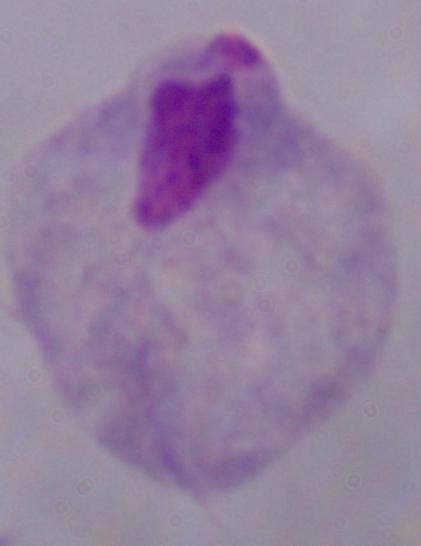

Summary:
  - Modality: photomicrograph
  - Identification: trichomonad
  - Magnification: 1000x